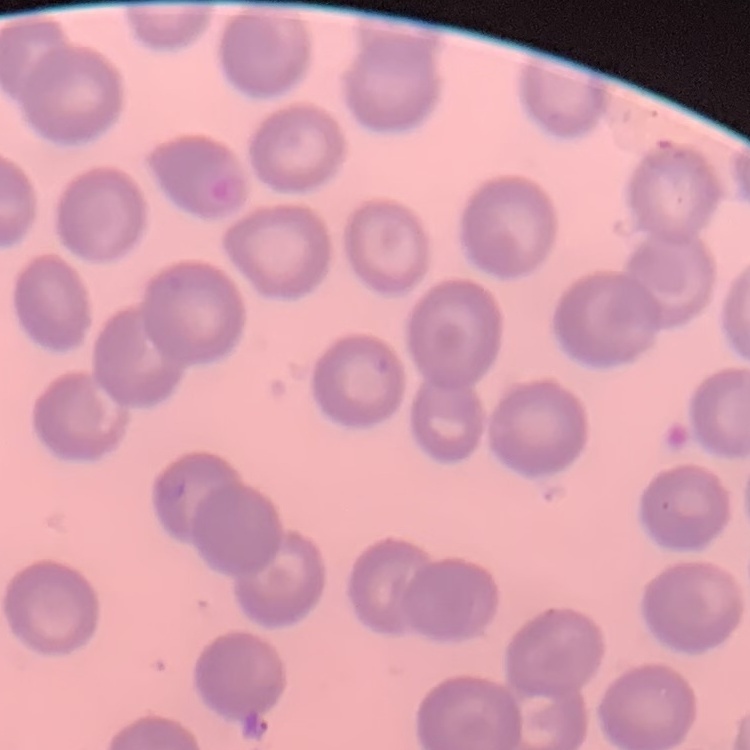 The erythrocytes exhibit no rouleaux formation. Thin peripheral smear. Stained with either Field's or Giemsa. One tile cut from a larger photomicrograph.